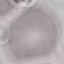 Malaria status: uninfected. Automatically extracted cell patch, resized to 64 × 64 pixels. Thin blood film. Giemsa-stained preparation. Acquired by smartphone through the microscope eyepiece.